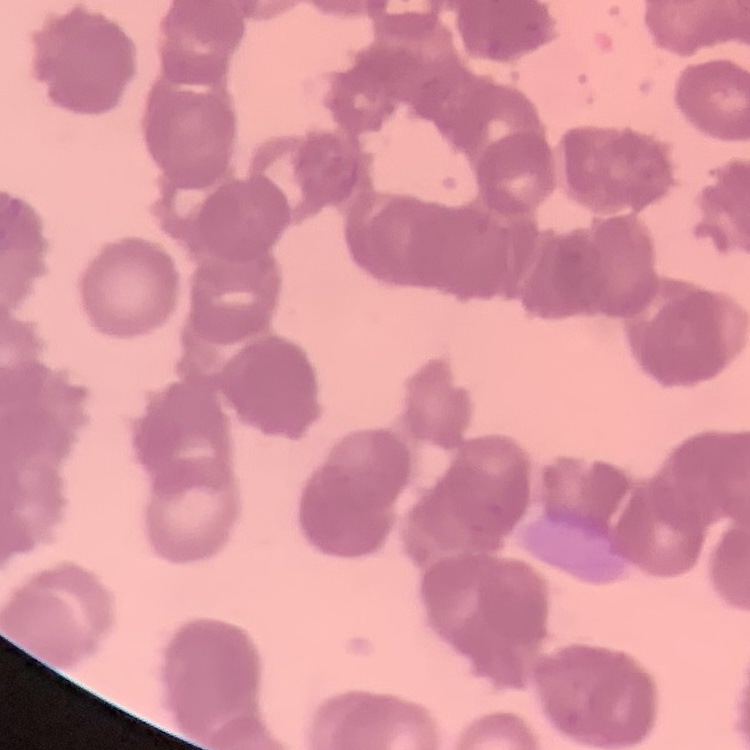

Summary:
  - Erythrocyte morphology: rouleaux formation
  - Stain: Field's or Giemsa
  - Preparation: thin peripheral smear
  - Image type: square crop of a larger photomicrograph